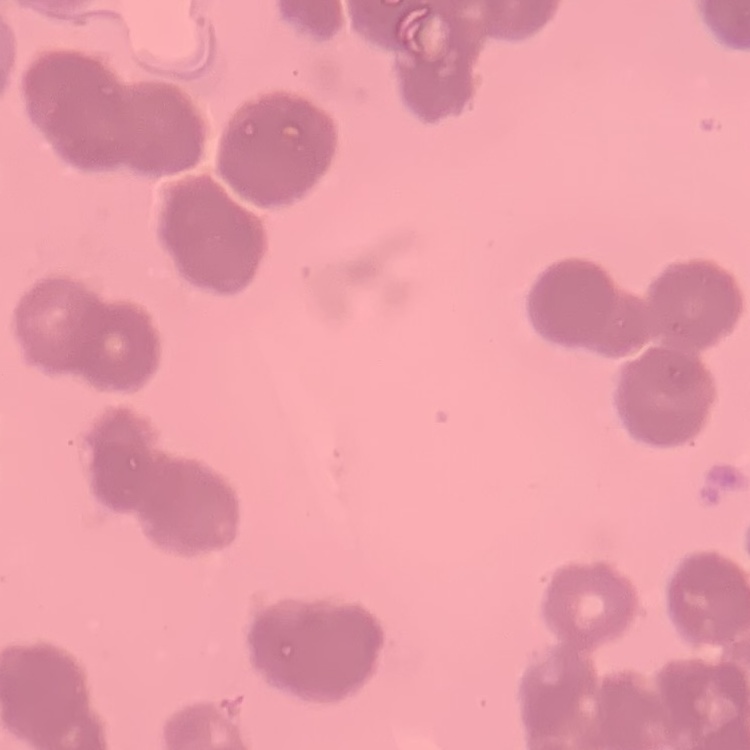
The erythrocytes show rouleaux formation. Square crop of a larger photomicrograph. Field's or Giemsa stain. Thin blood smear.